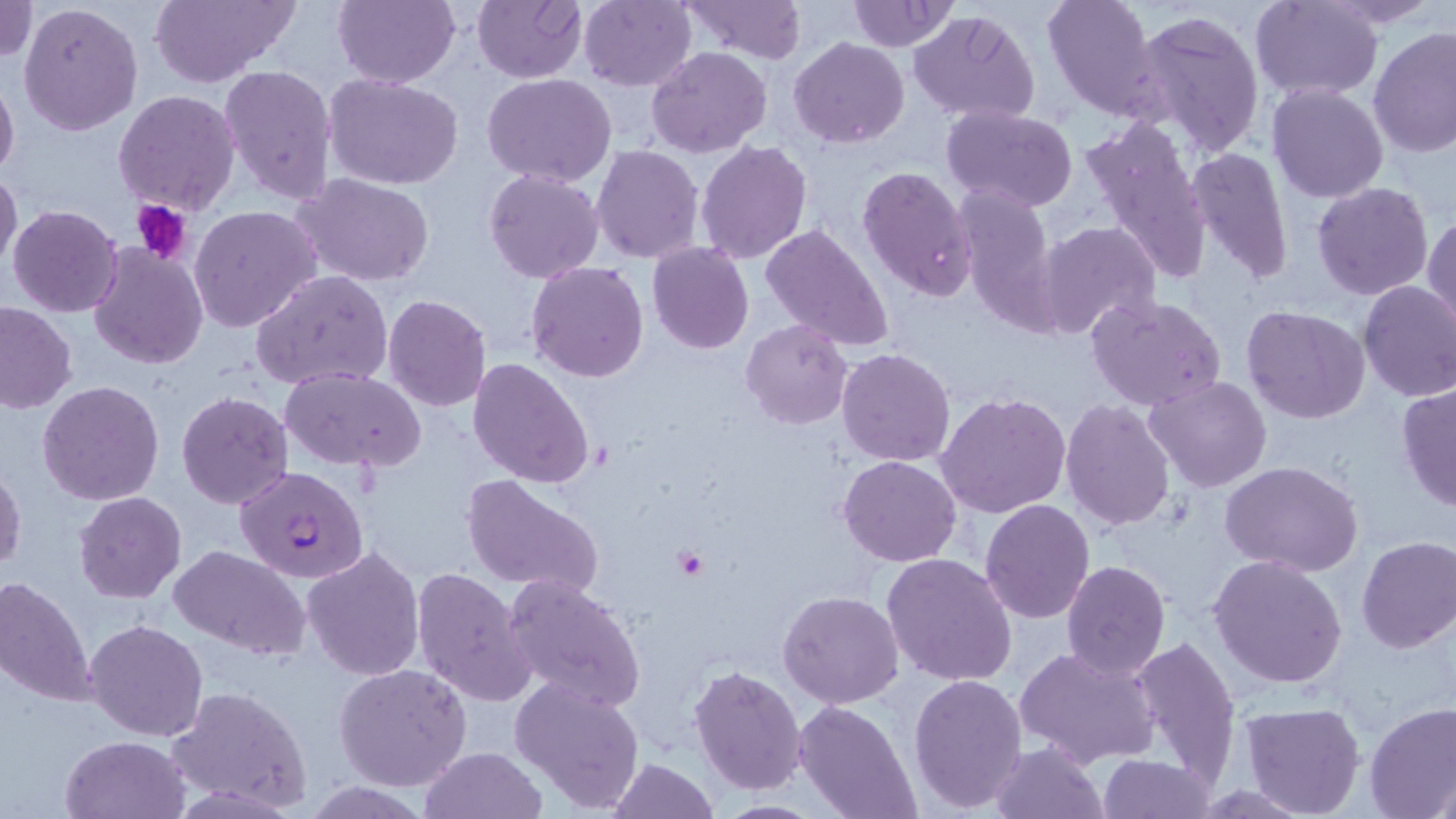

slide-level diagnosis = Plasmodium falciparum
modality = optical microscopy
Plasmodium falciparum-infected red blood cell locations = approximate bounding boxes as [x1, y1, x2, y2] in pixels: [235, 464, 369, 584]
preparation = thin blood film
platelet locations = approximate bounding boxes as [x1, y1, x2, y2] in pixels: [132, 198, 193, 266], [671, 546, 709, 581]
image size = 1456×819 pixels
stain = May-Grünwald-Giemsa
magnification = 1000x
field of view = one of a larger specimen
uninfected red blood cell locations = approximate bounding boxes as [x1, y1, x2, y2] in pixels: [0, 0, 39, 63], [148, 0, 300, 86], [333, 0, 459, 88], [473, 0, 588, 83], [680, 0, 808, 62], [847, 0, 960, 52], [1041, 0, 1159, 121], [1252, 0, 1384, 100], [1322, 0, 1444, 28], [577, 1, 697, 90], [19, 4, 143, 136], [907, 9, 1040, 126], [1132, 10, 1265, 156], [1369, 27, 1455, 158], [790, 36, 910, 148], [647, 46, 772, 158], [219, 63, 337, 206], [0, 72, 19, 183], [323, 73, 464, 189], [483, 74, 617, 188], [1267, 84, 1387, 203], [113, 90, 240, 213], [939, 106, 1079, 213], [1077, 115, 1211, 289], [696, 140, 812, 263], [591, 144, 705, 264], [1186, 146, 1295, 289], [857, 165, 977, 302], [0, 168, 22, 278], [484, 168, 605, 284], [292, 173, 436, 287], [1313, 181, 1434, 300], [956, 184, 1061, 337], [7, 204, 123, 317], [190, 205, 321, 334], [1424, 215, 1456, 332], [1037, 221, 1161, 344], [761, 223, 896, 353], [88, 242, 209, 369], [648, 242, 753, 354], [526, 263, 648, 383], [251, 269, 393, 391], [1358, 281, 1456, 403], [383, 293, 493, 411], [1086, 293, 1227, 411], [0, 300, 78, 413], [1242, 306, 1368, 424], [740, 319, 853, 430], [836, 347, 956, 466], [468, 358, 596, 488], [280, 368, 426, 472], [1144, 375, 1274, 493], [37, 380, 165, 505], [1395, 381, 1456, 513], [176, 390, 295, 509], [937, 390, 1071, 520], [1061, 400, 1178, 533], [839, 454, 962, 567], [1221, 461, 1363, 577], [0, 465, 26, 573], [461, 474, 606, 601], [74, 492, 187, 605], [980, 498, 1095, 623], [1356, 536, 1456, 654], [170, 546, 311, 660], [302, 546, 427, 682], [882, 553, 1019, 686], [1208, 555, 1348, 689], [1062, 560, 1170, 680], [411, 567, 536, 708], [500, 574, 644, 712], [1, 576, 96, 708], [778, 590, 903, 709], [85, 618, 208, 741], [1131, 636, 1241, 787], [1014, 644, 1161, 770], [689, 663, 809, 796], [334, 664, 474, 792], [909, 673, 1028, 813], [510, 674, 646, 813], [169, 685, 312, 812], [795, 701, 922, 819], [1363, 701, 1456, 818], [1238, 702, 1366, 818], [61, 734, 189, 818], [989, 741, 1108, 818], [419, 746, 546, 818], [1098, 754, 1216, 817], [607, 758, 720, 818], [1429, 764, 1455, 817]